Point out each malaria parasite.
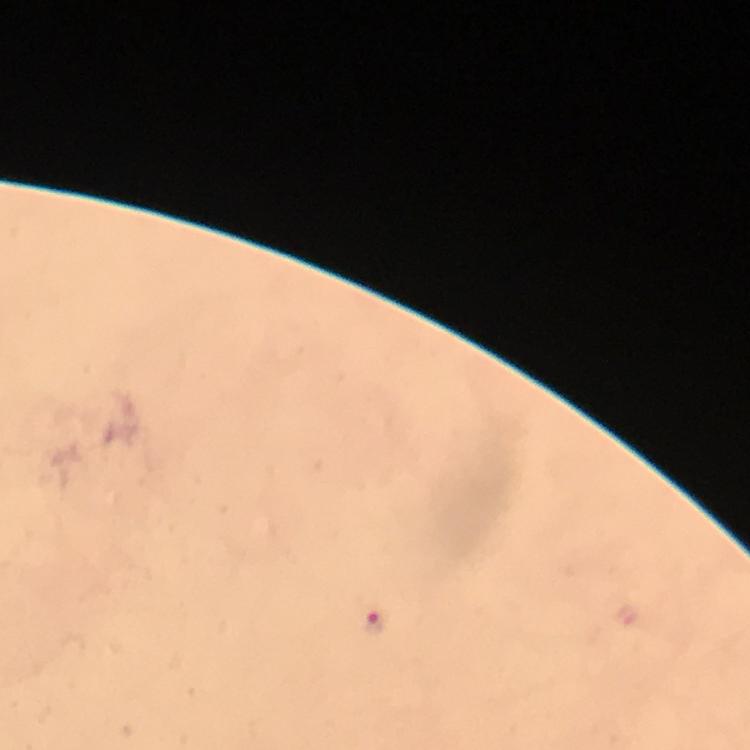

Approximate centers as [x, y] in pixels.
Malaria parasites: [374, 624].

cropped from = a single field of view
context = from a diagnostic examination for malaria
preparation = thick smear
image size = 750×750 pixels
stain = Giemsa
capture = smartphone mounted on the microscope
immersion oil = used
magnification = 100x